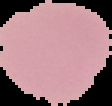 Result: no malaria parasites detected. From a thin blood film. Image is 112×106 pixels. Segmented cell region on a black background.